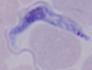

Summary:
  - Magnification: 1000x
  - Identification: trypanosome
  - Modality: photomicrograph